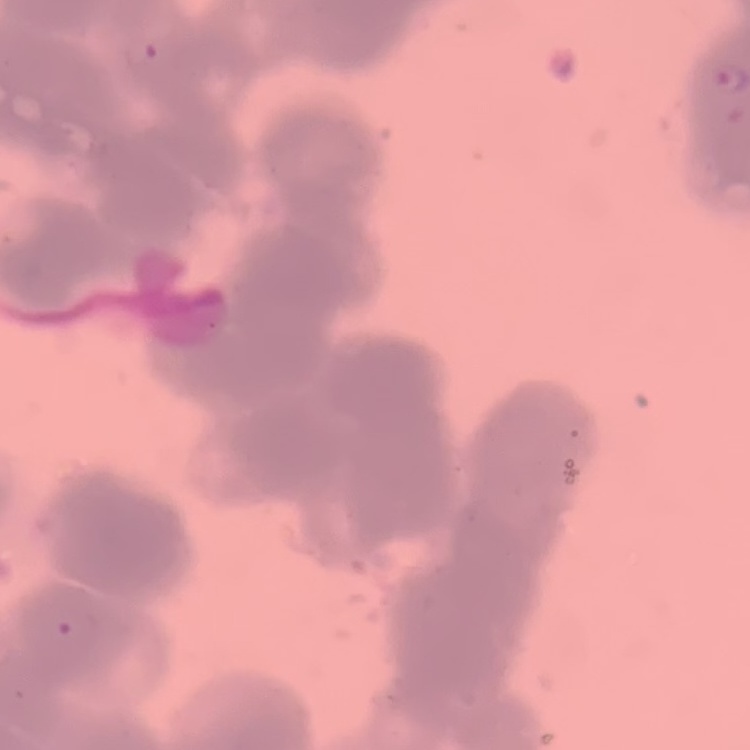

Summary:
  - Red blood cell morphology: rouleaux formation
  - Stain: Field's or Giemsa
  - Preparation: thin blood film
  - Image type: one tile cut from a larger photomicrograph